Comment on the morphology of the red blood cells.
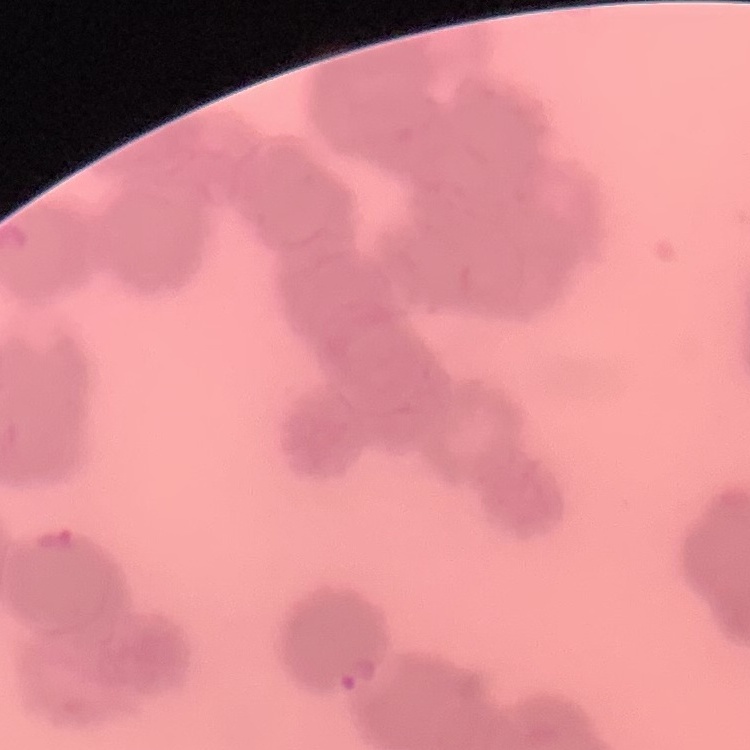
Rouleaux formation.

Summary:
  - Preparation: thin peripheral smear
  - Stain: Field's or Giemsa
  - Image type: square crop of a larger photomicrograph